Give the position of every Plasmodium parasite visible.
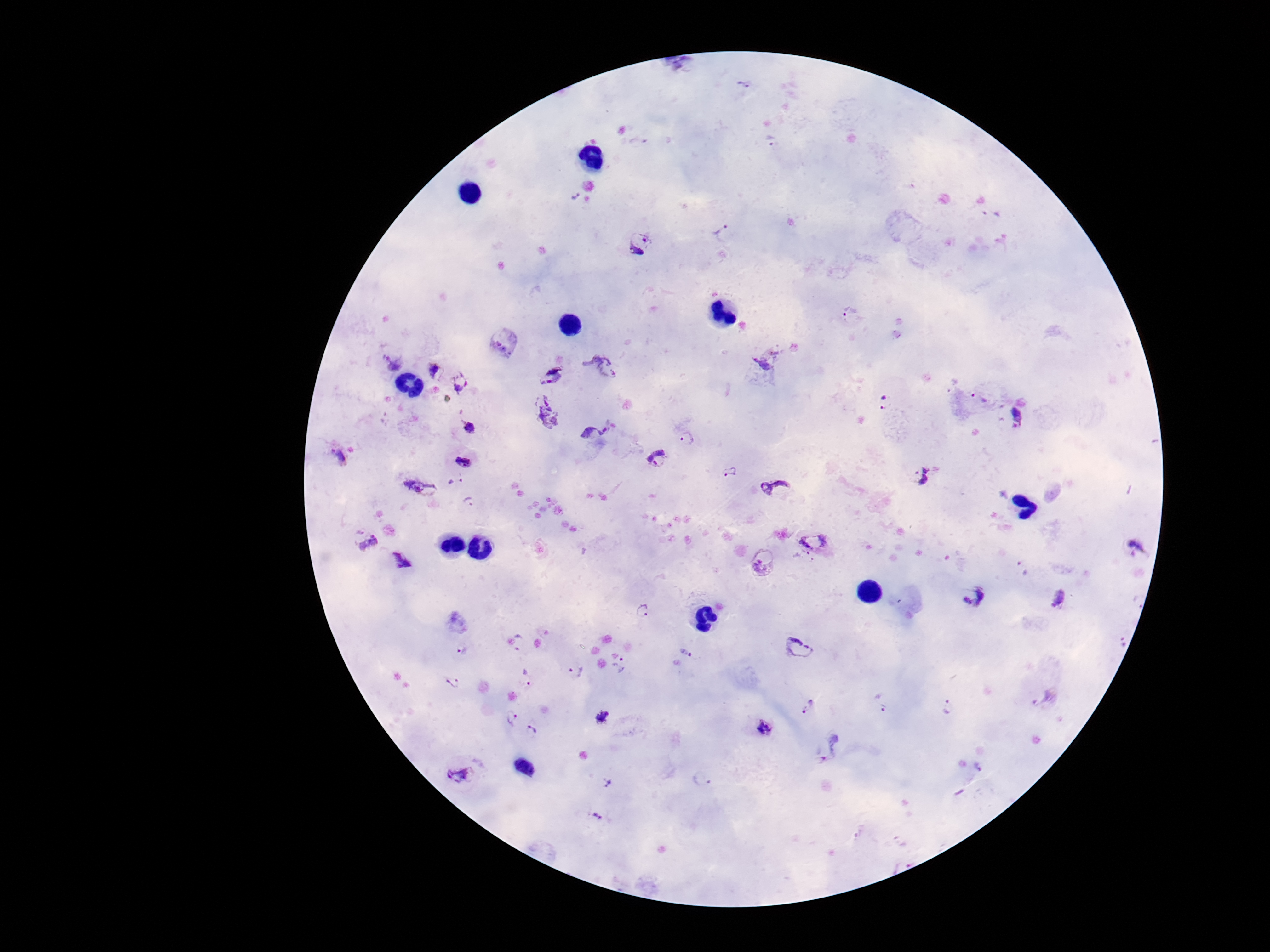
Approximate object centers, in pixels from the top-left corner.
Plasmodium parasites: (x=744, y=85), (x=771, y=141), (x=575, y=197), (x=723, y=234), (x=640, y=242), (x=850, y=312), (x=505, y=343), (x=768, y=358), (x=392, y=362), (x=602, y=365), (x=435, y=371), (x=553, y=374), (x=458, y=382), (x=978, y=399), (x=884, y=402), (x=547, y=412), (x=1018, y=417), (x=469, y=427), (x=593, y=431), (x=687, y=438), (x=340, y=456), (x=656, y=458), (x=464, y=461), (x=730, y=472), (x=924, y=477), (x=456, y=483), (x=420, y=487), (x=775, y=487), (x=470, y=502), (x=364, y=541), (x=814, y=542), (x=1137, y=548), (x=401, y=560), (x=765, y=563), (x=1022, y=570), (x=972, y=595), (x=1059, y=597), (x=644, y=611), (x=1118, y=639), (x=520, y=643), (x=799, y=649), (x=463, y=650), (x=686, y=651), (x=619, y=666), (x=575, y=672), (x=526, y=677), (x=454, y=683), (x=1043, y=696), (x=882, y=702), (x=949, y=706), (x=809, y=707), (x=512, y=716), (x=602, y=718), (x=764, y=727), (x=534, y=729), (x=830, y=748), (x=461, y=773), (x=701, y=779), (x=609, y=784), (x=596, y=818).

Smartphone photograph taken through the microscope eyepiece. Patient malaria status: positive. Thick blood smear. Giemsa stain. 100x magnification. Image is 1270×952 pixels. Single field of view.